Identify the blood parasite species.
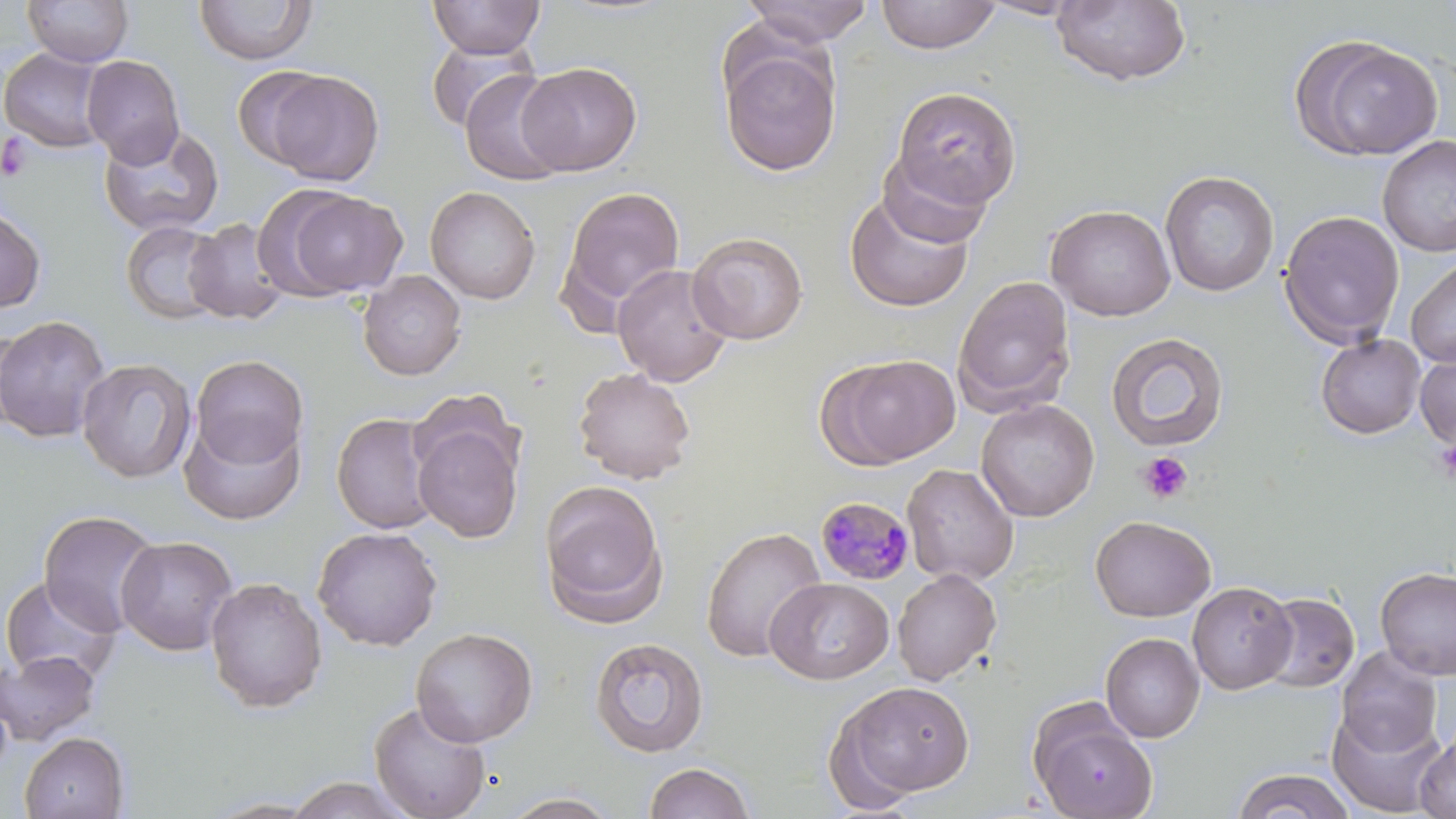

Plasmodium malariae.

field of view = single
uninfected red blood cell locations = approximate bounding boxes as [x1, y1, x2, y2] in pixels: [22, 0, 134, 67], [429, 0, 546, 58], [740, 0, 875, 46], [875, 0, 1002, 54], [977, 0, 1091, 20], [1051, 0, 1192, 87], [194, 1, 317, 65], [1291, 34, 1443, 162], [425, 37, 538, 133], [718, 40, 842, 177], [0, 47, 109, 153], [82, 55, 185, 167], [517, 62, 643, 176], [232, 65, 335, 168], [459, 68, 571, 186], [264, 70, 384, 185], [890, 86, 1021, 209], [98, 124, 223, 238], [1377, 135, 1456, 257], [877, 151, 993, 248], [1160, 170, 1280, 297], [425, 186, 541, 304], [559, 186, 686, 319], [282, 189, 408, 297], [844, 190, 976, 312], [0, 204, 45, 313], [1045, 204, 1176, 322], [1278, 209, 1405, 348], [184, 218, 290, 324], [121, 220, 227, 323], [687, 231, 808, 345], [1406, 257, 1456, 369], [612, 263, 734, 387], [357, 271, 466, 381], [952, 275, 1076, 416], [0, 315, 111, 443], [1105, 331, 1230, 452], [1315, 333, 1426, 439], [1415, 352, 1456, 450], [190, 354, 309, 470], [824, 354, 961, 468], [76, 358, 196, 483], [573, 367, 696, 484], [975, 398, 1099, 522], [331, 412, 440, 534], [411, 412, 525, 543], [180, 414, 306, 526], [902, 463, 1019, 586], [538, 479, 669, 627], [37, 510, 162, 636], [1090, 514, 1217, 621], [311, 526, 443, 651], [700, 526, 828, 663], [115, 534, 238, 655], [1375, 566, 1456, 680], [891, 568, 1002, 685], [0, 576, 122, 685], [205, 576, 327, 713], [765, 577, 893, 684], [1187, 582, 1297, 694], [1257, 592, 1359, 692], [410, 626, 538, 747], [1100, 633, 1204, 742], [589, 637, 709, 758], [1336, 647, 1443, 758], [0, 650, 101, 746], [830, 680, 977, 804], [369, 700, 492, 819], [1328, 708, 1448, 817], [1032, 716, 1158, 819], [1414, 729, 1456, 819], [19, 732, 129, 819], [643, 761, 757, 818], [1231, 768, 1356, 819], [282, 775, 419, 818], [498, 791, 622, 818]
stain = May-Grünwald-Giemsa
magnification = 1000x
preparation = thin blood film
image size = 1456×819 pixels
modality = optical microscopy
Plasmodium malariae-infected red blood cell locations = approximate bounding boxes as [x1, y1, x2, y2] in pixels: [815, 496, 915, 585]
platelet locations = approximate bounding boxes as [x1, y1, x2, y2] in pixels: [1, 133, 33, 181], [1435, 438, 1456, 484], [1138, 452, 1193, 504]